Identify the parasite.
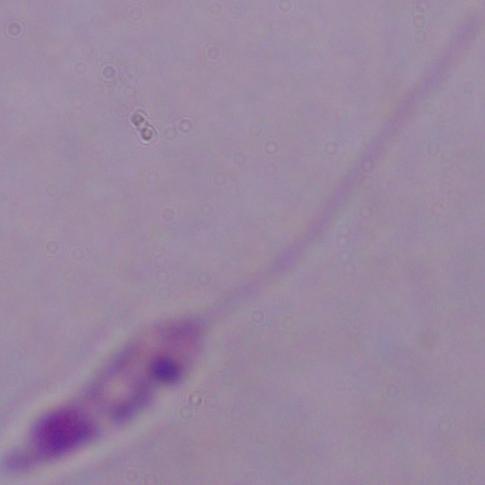
Leishmania.

Summary:
  - Magnification: 1000x
  - Modality: photomicrograph